Give the extent of all Plasmodium malariae-infected red blood cells.
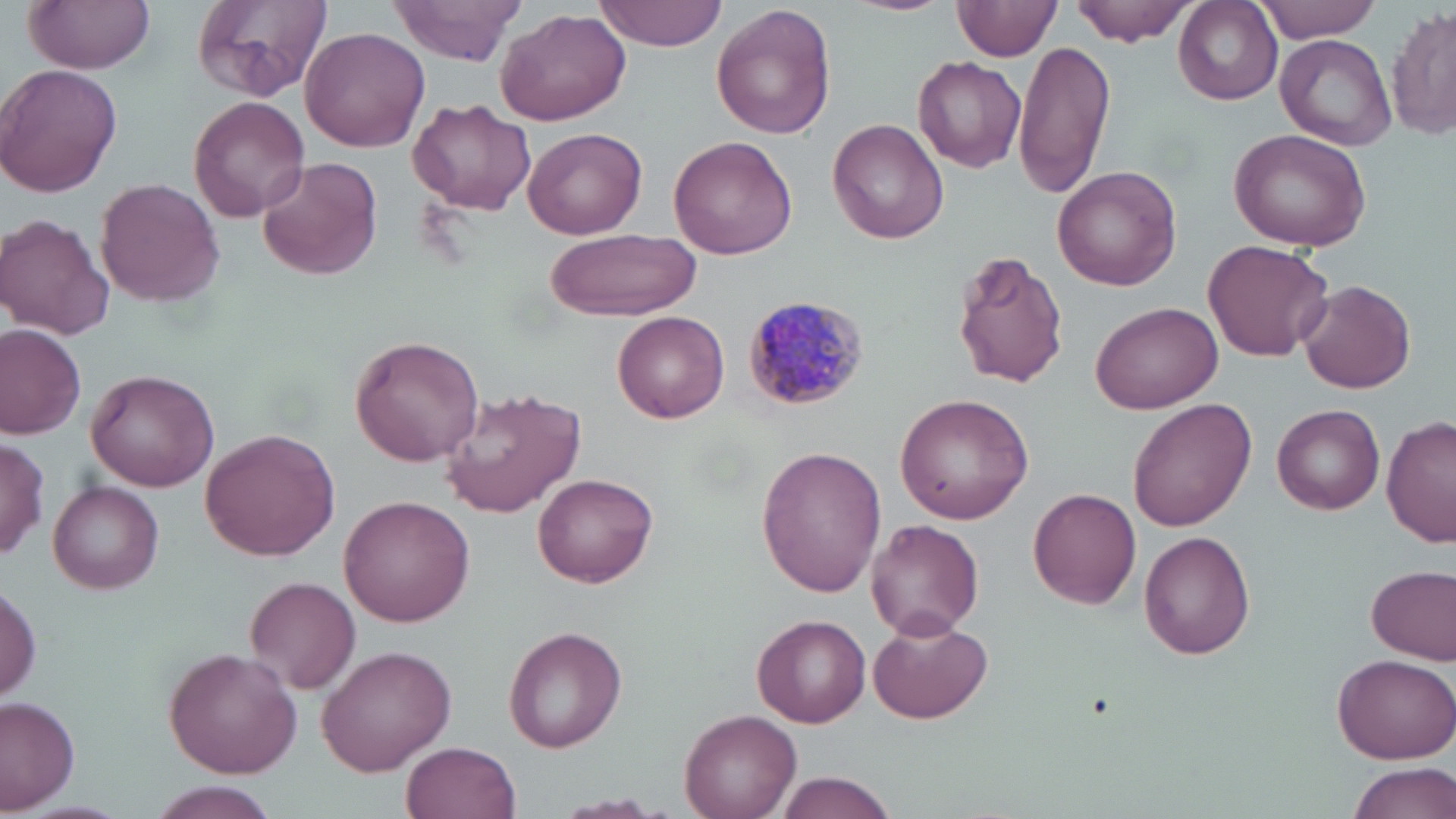
Approximate bounding boxes as [x1, y1, x2, y2] in pixels.
Plasmodium malariae-infected red blood cells: [741, 296, 869, 411].

Summary:
  - Uninfected red blood cell locations: [23, 0, 158, 72], [188, 0, 334, 104], [599, 0, 732, 50], [845, 0, 955, 16], [1071, 0, 1201, 44], [1255, 0, 1384, 42], [385, 1, 528, 65], [953, 2, 1063, 64], [1173, 3, 1283, 106], [710, 4, 837, 142], [495, 8, 631, 126], [1389, 9, 1455, 142], [302, 27, 430, 151], [1276, 34, 1397, 149], [1014, 40, 1117, 198], [912, 57, 1028, 173], [0, 63, 123, 198], [188, 96, 310, 223], [406, 100, 537, 214], [827, 117, 948, 245], [523, 127, 647, 239], [1228, 127, 1372, 251], [668, 136, 799, 260], [258, 156, 383, 281], [1052, 165, 1182, 292], [94, 177, 224, 306], [0, 214, 114, 341], [546, 227, 700, 322], [1202, 239, 1331, 363], [565, 240, 710, 385], [951, 253, 1068, 390], [1296, 280, 1417, 394], [1090, 302, 1224, 415], [612, 311, 729, 423], [0, 325, 87, 437], [349, 335, 482, 467], [86, 369, 220, 494], [441, 387, 588, 518], [895, 393, 1034, 525], [1127, 399, 1258, 534], [1271, 404, 1386, 514], [1382, 415, 1456, 549], [200, 427, 339, 562], [0, 438, 48, 560], [756, 447, 887, 599], [534, 472, 657, 587], [49, 481, 163, 594], [1029, 488, 1142, 608], [340, 494, 477, 626], [865, 519, 983, 640], [1139, 530, 1256, 660], [1368, 564, 1456, 666], [243, 577, 360, 693], [0, 581, 42, 704], [868, 615, 994, 726], [753, 616, 871, 727], [504, 627, 628, 755], [317, 645, 457, 776], [163, 647, 301, 779], [1329, 651, 1456, 764], [0, 697, 81, 813], [680, 708, 801, 817], [402, 740, 521, 819], [1343, 761, 1455, 819], [770, 770, 900, 819], [149, 785, 277, 819], [555, 793, 666, 815]
  - Slide-level diagnosis: Plasmodium malariae
  - Field of view: single
  - Preparation: thin blood smear
  - Image size: 1456×819 pixels
  - Modality: light microscopy
  - Stain: May-Grünwald-Giemsa
  - Magnification: 1000x